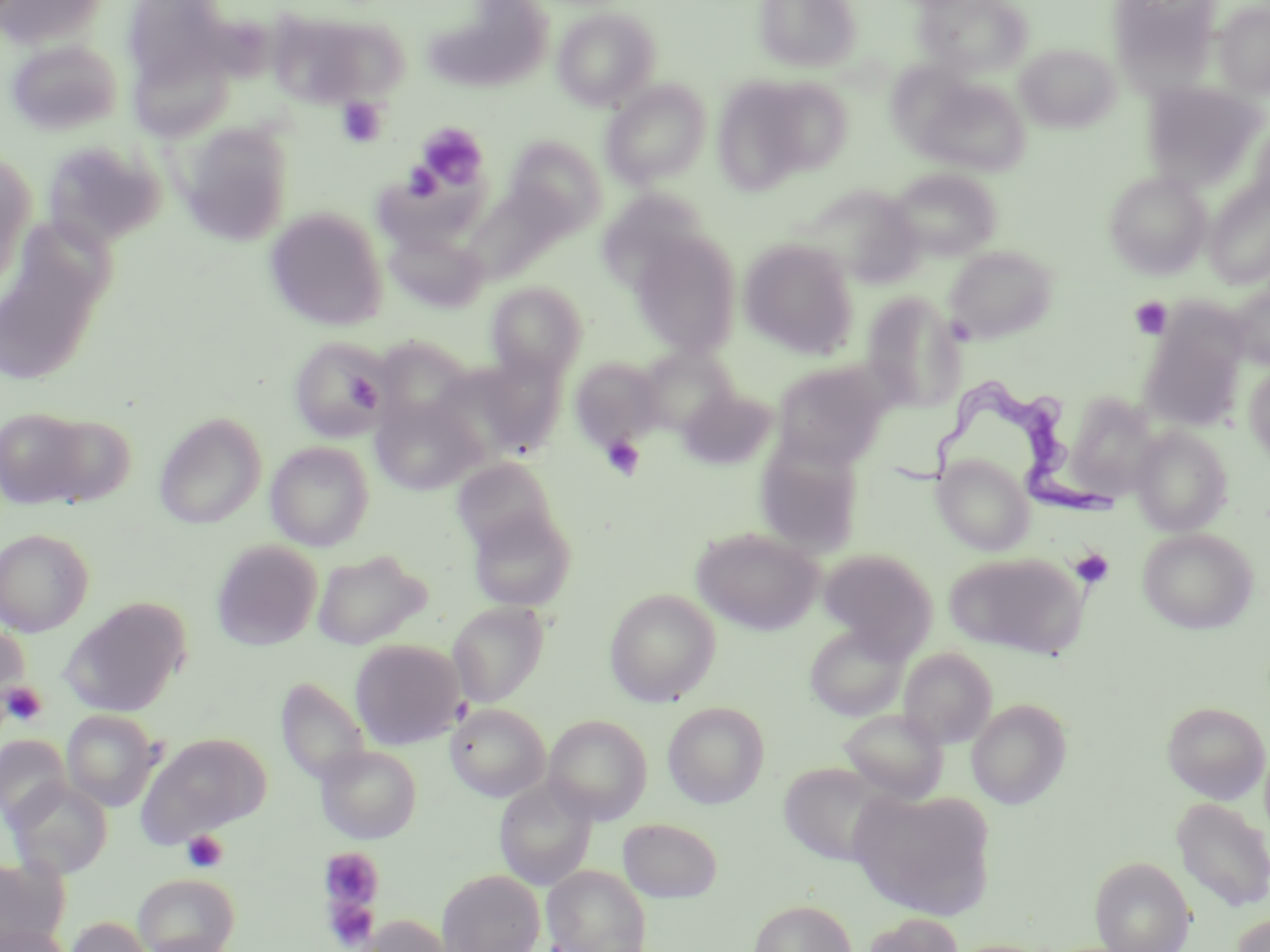

Summary:
  - Coordinate format: approximate bounding boxes as [x1, y1, x2, y2] in pixels
  - Platelet locations: [337, 97, 388, 147], [416, 122, 489, 192], [403, 160, 444, 203], [1130, 296, 1173, 339], [345, 374, 382, 411], [600, 435, 646, 481], [1071, 548, 1114, 589], [2, 681, 48, 728], [181, 830, 229, 874], [319, 847, 385, 915], [327, 896, 378, 950]
  - Uninfected red blood cell locations: [1, 0, 109, 50], [120, 0, 243, 111], [754, 0, 861, 72], [915, 0, 1033, 77], [1107, 0, 1222, 85], [1214, 1, 1270, 99], [424, 3, 552, 92], [265, 5, 398, 107], [552, 6, 660, 110], [5, 39, 122, 136], [1015, 43, 1120, 133], [886, 60, 978, 153], [717, 76, 839, 184], [916, 77, 1031, 176], [601, 80, 711, 187], [1142, 82, 1267, 190], [1245, 120, 1270, 219], [178, 122, 294, 246], [504, 136, 607, 236], [41, 139, 167, 250], [0, 152, 35, 284], [888, 168, 1001, 261], [1104, 171, 1211, 279], [1204, 183, 1270, 289], [463, 184, 572, 283], [801, 184, 925, 286], [597, 188, 712, 292], [264, 207, 389, 331], [0, 228, 111, 385], [384, 229, 489, 313], [630, 232, 741, 359], [738, 238, 860, 358], [943, 245, 1057, 344], [486, 281, 587, 380], [1229, 283, 1270, 368], [861, 291, 967, 412], [1139, 321, 1247, 432], [289, 337, 388, 443], [637, 346, 738, 436], [441, 355, 566, 463], [569, 357, 666, 448], [770, 360, 892, 468], [1244, 364, 1270, 464], [678, 386, 776, 471], [1064, 392, 1163, 501], [371, 396, 483, 495], [0, 406, 97, 509], [32, 413, 136, 509], [155, 413, 266, 529], [1130, 427, 1233, 536], [756, 440, 863, 556], [265, 441, 374, 550], [933, 455, 1034, 555], [452, 457, 558, 552], [466, 507, 577, 612], [0, 528, 94, 636], [691, 528, 823, 634], [1137, 528, 1259, 634], [210, 539, 322, 651], [312, 548, 431, 649], [819, 548, 938, 657], [945, 551, 1086, 658], [604, 587, 721, 706], [59, 597, 191, 717], [447, 601, 550, 708], [0, 620, 30, 717], [803, 623, 910, 721], [349, 638, 466, 749], [898, 647, 997, 749], [277, 680, 368, 780], [967, 698, 1072, 809], [662, 701, 770, 809], [1162, 701, 1269, 803], [446, 703, 550, 801], [839, 708, 949, 803], [61, 709, 162, 812], [544, 715, 653, 824], [138, 733, 271, 841], [0, 735, 71, 826], [316, 743, 422, 843], [778, 761, 895, 866], [7, 778, 113, 879], [494, 778, 597, 891], [850, 788, 994, 919], [1172, 798, 1270, 912], [617, 818, 723, 903], [1090, 856, 1195, 952], [0, 857, 69, 949], [543, 864, 651, 952], [438, 869, 545, 952], [133, 873, 239, 952], [749, 899, 857, 952], [861, 912, 964, 952], [1230, 913, 1270, 952], [354, 914, 457, 952], [63, 916, 153, 952], [0, 924, 71, 952], [141, 933, 239, 952]
  - Trypanosoma brucei locations: [878, 375, 1122, 522]
  - Slide-level diagnosis: Trypanosoma brucei
  - Field of view: single
  - Preparation: thin blood smear
  - Image size: 1270×952 pixels
  - Modality: optical microscopy
  - Stain: May-Grünwald-Giemsa
  - Magnification: 1000x